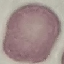
result = no malaria parasites detected
capture = smartphone through the microscope eyepiece
preparation = thin blood smear
stain = Giemsa
image type = automatically extracted cell patch, resized to 64 × 64 pixels